Locate every blood parasite and identify its species.
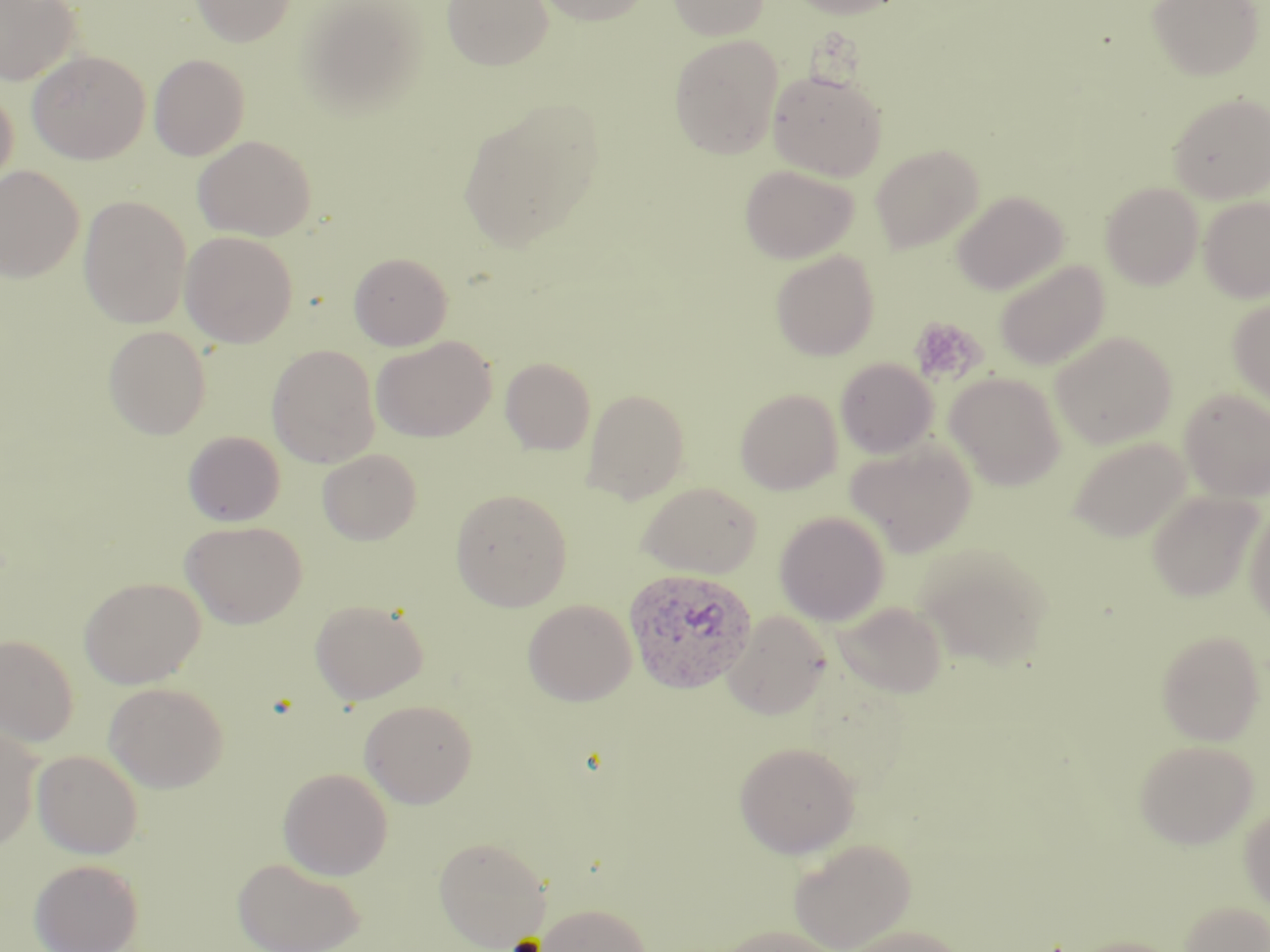

Approximate bounding boxes as named x1/y1/x2/y2 corners in pixels.
Plasmodium ovale-infected red blood cells: (x1=623, y1=567, x2=758, y2=694).
No Plasmodium falciparum, Plasmodium malariae, Plasmodium vivax, Babesia divergens, or Trypanosoma brucei observed.

Platelet locations: (x1=909, y1=317, x2=985, y2=386). Uninfected red blood cell locations: (x1=0, y1=0, x2=81, y2=85), (x1=190, y1=0, x2=296, y2=47), (x1=442, y1=0, x2=553, y2=70), (x1=534, y1=0, x2=654, y2=26), (x1=668, y1=0, x2=769, y2=39), (x1=784, y1=0, x2=907, y2=18), (x1=1147, y1=0, x2=1264, y2=81), (x1=298, y1=1, x2=427, y2=118), (x1=669, y1=35, x2=784, y2=159), (x1=27, y1=50, x2=150, y2=163), (x1=149, y1=54, x2=250, y2=161), (x1=768, y1=69, x2=887, y2=181), (x1=0, y1=88, x2=19, y2=197), (x1=1167, y1=91, x2=1270, y2=203), (x1=458, y1=103, x2=603, y2=251), (x1=192, y1=135, x2=316, y2=241), (x1=871, y1=144, x2=984, y2=253), (x1=739, y1=164, x2=859, y2=263), (x1=0, y1=165, x2=85, y2=282), (x1=1101, y1=182, x2=1203, y2=289), (x1=952, y1=191, x2=1068, y2=295), (x1=78, y1=196, x2=192, y2=328), (x1=1199, y1=196, x2=1270, y2=302), (x1=180, y1=231, x2=298, y2=347), (x1=770, y1=250, x2=879, y2=361), (x1=348, y1=251, x2=453, y2=350), (x1=994, y1=260, x2=1109, y2=370), (x1=1228, y1=297, x2=1270, y2=408), (x1=102, y1=325, x2=211, y2=439), (x1=1051, y1=331, x2=1178, y2=448), (x1=371, y1=336, x2=496, y2=442), (x1=266, y1=344, x2=381, y2=468), (x1=500, y1=357, x2=596, y2=455), (x1=835, y1=358, x2=938, y2=458), (x1=945, y1=372, x2=1066, y2=490), (x1=582, y1=388, x2=690, y2=503), (x1=735, y1=388, x2=842, y2=494), (x1=1179, y1=388, x2=1270, y2=501), (x1=182, y1=431, x2=285, y2=527), (x1=1068, y1=436, x2=1192, y2=542), (x1=846, y1=440, x2=977, y2=557), (x1=317, y1=449, x2=422, y2=545), (x1=636, y1=481, x2=761, y2=578), (x1=450, y1=489, x2=572, y2=611), (x1=1147, y1=490, x2=1264, y2=601), (x1=1245, y1=505, x2=1270, y2=627), (x1=774, y1=511, x2=890, y2=626), (x1=180, y1=521, x2=306, y2=628), (x1=917, y1=544, x2=1051, y2=669), (x1=79, y1=576, x2=206, y2=688), (x1=309, y1=598, x2=428, y2=704), (x1=523, y1=599, x2=637, y2=706), (x1=833, y1=601, x2=948, y2=698), (x1=723, y1=611, x2=831, y2=719), (x1=1156, y1=629, x2=1266, y2=745), (x1=0, y1=634, x2=78, y2=747), (x1=103, y1=681, x2=228, y2=792), (x1=359, y1=699, x2=478, y2=808), (x1=0, y1=725, x2=42, y2=851), (x1=1134, y1=739, x2=1258, y2=848), (x1=734, y1=741, x2=861, y2=858), (x1=32, y1=749, x2=144, y2=859), (x1=277, y1=766, x2=394, y2=880), (x1=1240, y1=804, x2=1270, y2=914), (x1=433, y1=835, x2=551, y2=950), (x1=788, y1=837, x2=916, y2=952), (x1=232, y1=856, x2=366, y2=952), (x1=29, y1=858, x2=144, y2=952), (x1=1178, y1=900, x2=1270, y2=951), (x1=535, y1=902, x2=652, y2=951), (x1=711, y1=925, x2=842, y2=952), (x1=838, y1=925, x2=968, y2=952), (x1=1068, y1=936, x2=1183, y2=952). Slide-level diagnosis: Plasmodium ovale. Image is 1270×952 pixels. 1000x magnification. Optical microscopy. One field of a larger specimen. May-Grünwald-Giemsa-stained preparation. Thin blood film.